Identify the parasite.
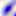
This is Toxoplasma gondii.

Micrograph. 400x magnification.